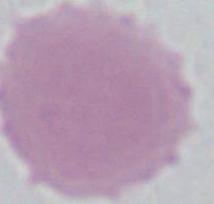
magnification = 1000x
identification = erythrocyte
modality = micrograph